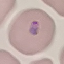

Result: malaria parasites detected. Giemsa-stained preparation. Thin blood smear. Automatically extracted cell patch, resized to 64 × 64 pixels. Acquired by smartphone through the microscope eyepiece.